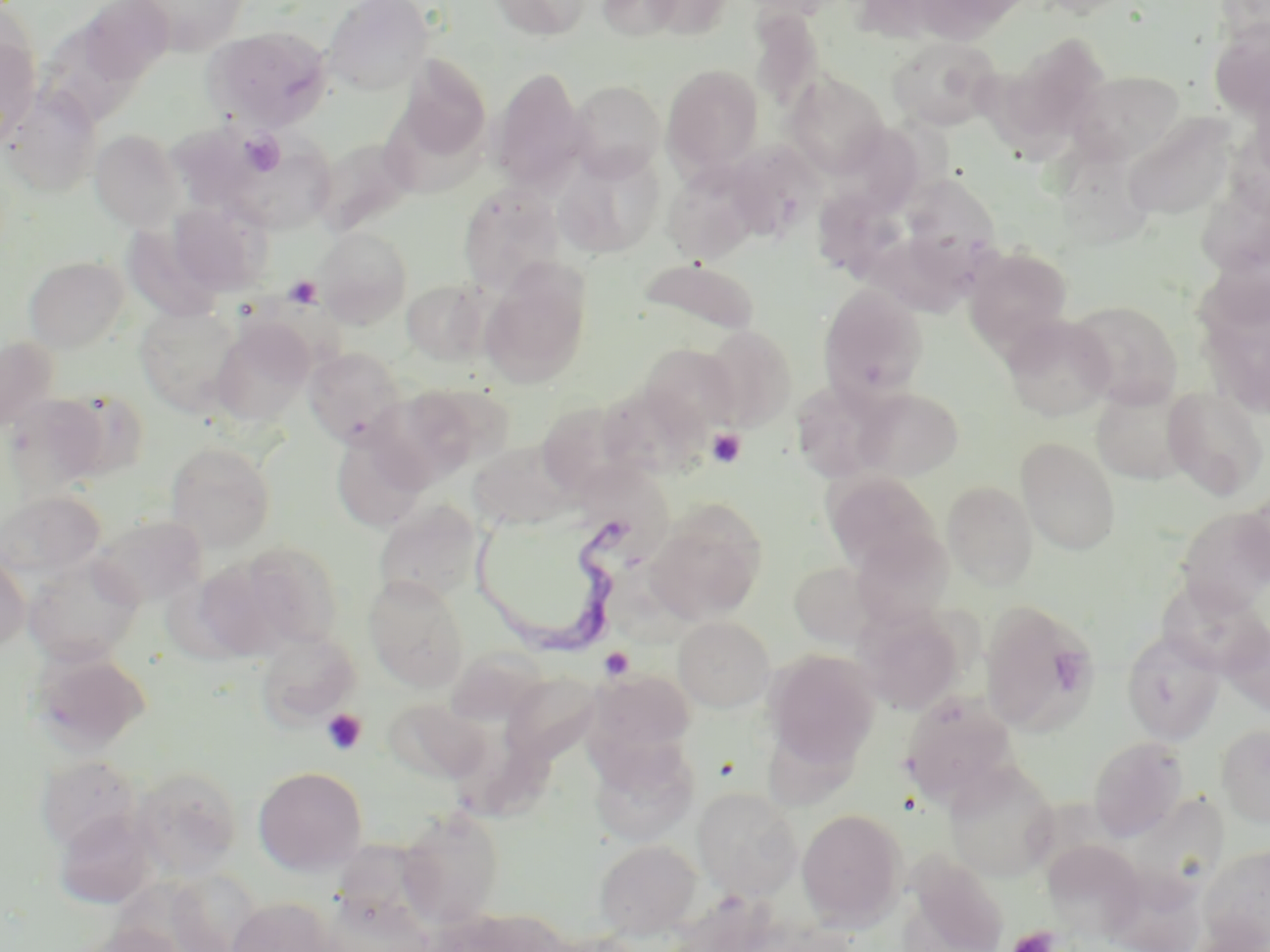

slide-level diagnosis = Trypanosoma brucei
uninfected red blood cell locations = approximate bounding boxes as (x1,y1)-(x2,y2) corner pairs in pixels: (76,0)-(174,88), (131,0)-(251,55), (323,0)-(433,95), (489,0)-(594,41), (597,0)-(684,42), (645,0)-(733,41), (910,0)-(1028,45), (750,11)-(825,111), (1209,22)-(1270,120), (37,23)-(145,134), (203,26)-(332,132), (0,27)-(40,143), (1004,32)-(1111,143), (887,35)-(1002,131), (397,56)-(492,162), (662,65)-(764,175), (490,67)-(589,195), (1068,71)-(1185,165), (785,72)-(889,177), (568,80)-(666,179), (2,88)-(101,196), (383,115)-(509,195), (1131,120)-(1245,227), (90,129)-(185,231), (225,135)-(336,235), (313,136)-(417,236), (726,141)-(825,239), (555,148)-(665,258), (663,162)-(762,265), (897,173)-(1002,284), (457,182)-(567,296), (815,187)-(916,275), (1197,187)-(1270,284), (169,201)-(271,295), (126,227)-(223,319), (314,227)-(413,327), (964,246)-(1072,353), (24,255)-(128,352), (638,258)-(759,340), (480,260)-(592,387), (401,279)-(489,365), (818,283)-(928,403), (1068,301)-(1183,407), (134,304)-(245,415), (1001,315)-(1116,421), (211,319)-(313,427), (702,325)-(797,431), (0,336)-(60,432), (640,343)-(739,436), (303,346)-(407,448), (791,379)-(899,484), (384,383)-(508,481), (1091,383)-(1196,485), (599,384)-(711,480), (850,387)-(964,481), (1162,387)-(1268,500), (55,389)-(151,482), (4,393)-(109,495), (536,402)-(635,498), (331,428)-(430,532), (1017,438)-(1121,555), (165,441)-(275,551), (468,441)-(575,530), (822,470)-(941,573), (943,481)-(1038,589), (1,490)-(105,581), (1240,491)-(1270,586), (374,499)-(484,606), (645,502)-(767,623), (1176,507)-(1270,613), (92,514)-(207,607), (851,530)-(953,628), (240,543)-(343,650), (0,552)-(30,653), (24,555)-(144,666), (189,555)-(300,662), (788,561)-(879,648), (364,574)-(470,692), (1155,578)-(1269,676), (980,602)-(1099,734), (853,608)-(964,714), (673,616)-(775,711), (1220,618)-(1270,717), (1121,630)-(1225,744), (254,631)-(360,728), (31,648)-(152,753), (764,649)-(880,770), (589,669)-(696,763), (502,673)-(602,764), (899,691)-(1020,804), (383,697)-(492,787), (1216,723)-(1270,827), (1087,736)-(1188,840), (587,737)-(700,846), (36,755)-(140,852), (944,761)-(1060,881), (130,765)-(243,878), (253,765)-(368,875), (693,787)-(803,899), (1139,791)-(1231,911), (398,806)-(504,928), (797,808)-(906,929), (54,811)-(155,909), (328,835)-(434,937), (594,839)-(702,940), (1043,839)-(1148,939), (1199,844)-(1270,951), (903,856)-(1009,952), (167,871)-(263,951), (227,897)-(337,952), (81,922)-(186,952)
image size = 1270×952 pixels
preparation = thin blood film
modality = light microscopy
Trypanosoma brucei locations = approximate bounding boxes as (x1,y1)-(x2,y2) corner pairs in pixels: (469,510)-(649,666)
magnification = 1000x
platelet locations = approximate bounding boxes as (x1,y1)-(x2,y2) corner pairs in pixels: (238,130)-(285,176), (284,275)-(322,309), (707,428)-(746,468), (599,647)-(634,680), (321,708)-(367,755), (1007,926)-(1059,952)
stain = May-Grünwald-Giemsa
field of view = one of a larger specimen